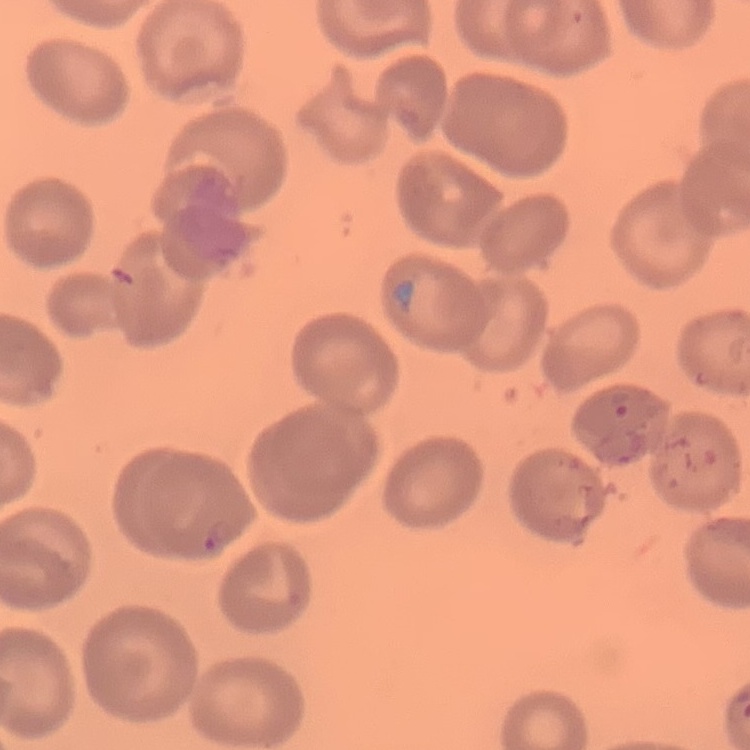
The red blood cells exhibit no rouleaux formation. Field's or Giemsa stain. Square crop of a larger photomicrograph. Thin peripheral smear.